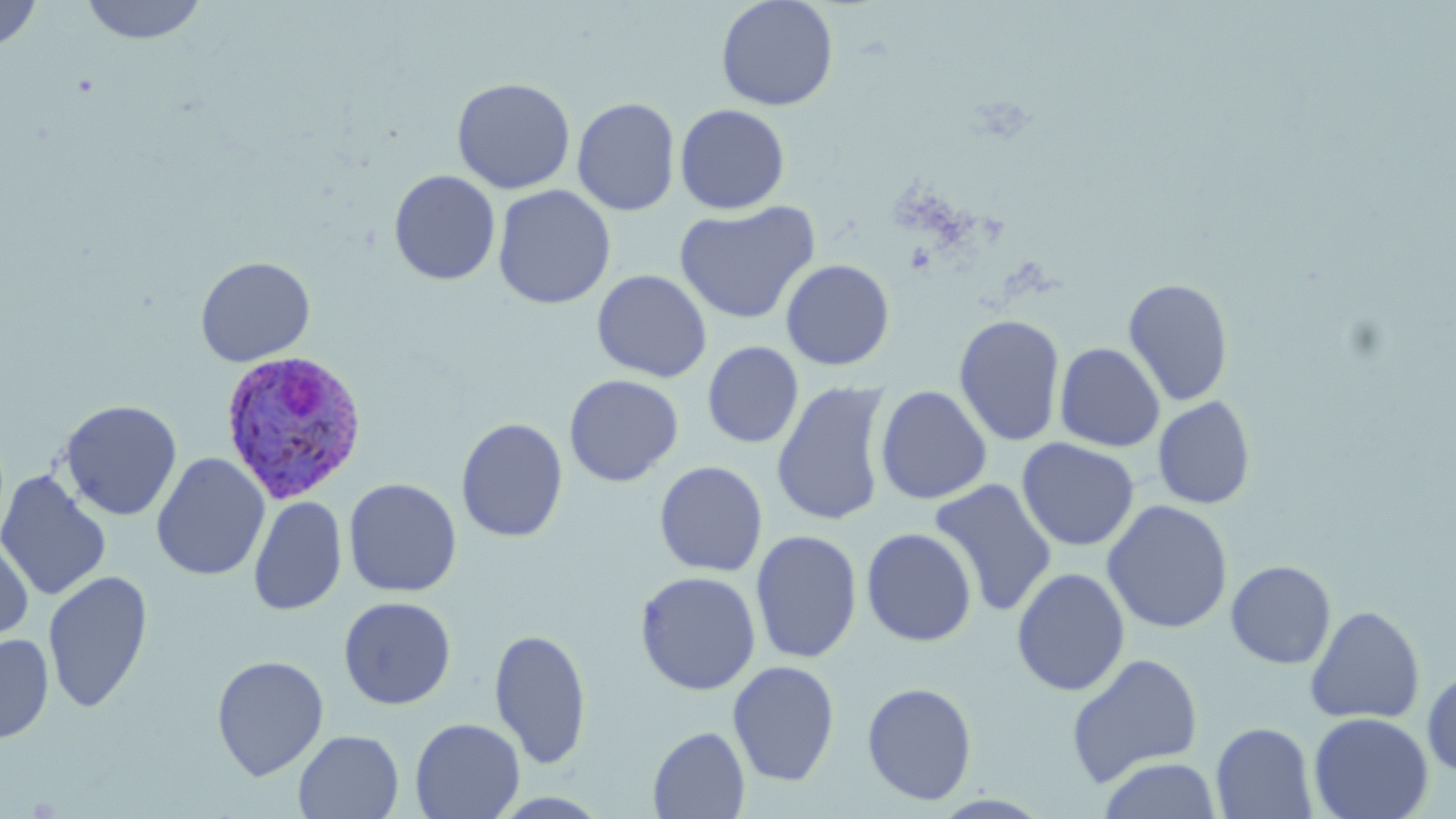 Approximate bounding boxes as named x1/y1/x2/y2 corners in pixels. Uninfected red blood cell locations: (x1=0, y1=0, x2=42, y2=52), (x1=80, y1=0, x2=208, y2=44), (x1=716, y1=0, x2=839, y2=111), (x1=451, y1=77, x2=576, y2=194), (x1=571, y1=97, x2=681, y2=216), (x1=674, y1=103, x2=791, y2=214), (x1=389, y1=170, x2=500, y2=285), (x1=493, y1=184, x2=616, y2=309), (x1=674, y1=201, x2=820, y2=325), (x1=194, y1=255, x2=316, y2=367), (x1=780, y1=258, x2=895, y2=371), (x1=592, y1=269, x2=712, y2=382), (x1=1122, y1=276, x2=1235, y2=407), (x1=953, y1=313, x2=1066, y2=447), (x1=702, y1=341, x2=804, y2=448), (x1=1054, y1=342, x2=1165, y2=452), (x1=564, y1=374, x2=684, y2=487), (x1=771, y1=380, x2=891, y2=527), (x1=875, y1=385, x2=992, y2=504), (x1=1152, y1=395, x2=1257, y2=510), (x1=58, y1=399, x2=183, y2=521), (x1=456, y1=417, x2=569, y2=543), (x1=1017, y1=437, x2=1140, y2=551), (x1=151, y1=453, x2=270, y2=581), (x1=654, y1=460, x2=768, y2=577), (x1=0, y1=470, x2=112, y2=601), (x1=928, y1=477, x2=1057, y2=616), (x1=343, y1=478, x2=462, y2=597), (x1=248, y1=495, x2=347, y2=617), (x1=1102, y1=499, x2=1233, y2=634), (x1=861, y1=527, x2=978, y2=647), (x1=750, y1=529, x2=863, y2=664), (x1=0, y1=535, x2=35, y2=644), (x1=1225, y1=559, x2=1336, y2=669), (x1=1012, y1=567, x2=1130, y2=696), (x1=42, y1=570, x2=154, y2=712), (x1=635, y1=570, x2=761, y2=695), (x1=338, y1=596, x2=457, y2=709), (x1=1305, y1=605, x2=1425, y2=725), (x1=489, y1=627, x2=592, y2=769), (x1=0, y1=633, x2=54, y2=744), (x1=1066, y1=652, x2=1205, y2=786), (x1=211, y1=655, x2=329, y2=780), (x1=727, y1=660, x2=841, y2=786), (x1=1422, y1=666, x2=1456, y2=779), (x1=861, y1=681, x2=978, y2=806), (x1=1080, y1=700, x2=1215, y2=819), (x1=1308, y1=712, x2=1433, y2=819), (x1=410, y1=717, x2=524, y2=819), (x1=1211, y1=722, x2=1318, y2=818), (x1=648, y1=726, x2=750, y2=818), (x1=294, y1=730, x2=404, y2=819), (x1=1096, y1=756, x2=1223, y2=819). Plasmodium ovale-infected red blood cell locations: (x1=218, y1=349, x2=369, y2=505). Slide-level diagnosis: Plasmodium ovale. Image is 1456×819 pixels. May-Grünwald-Giemsa stain. Light microscopy. Captured at 1000x magnification. Thin blood smear. One field of a larger specimen.